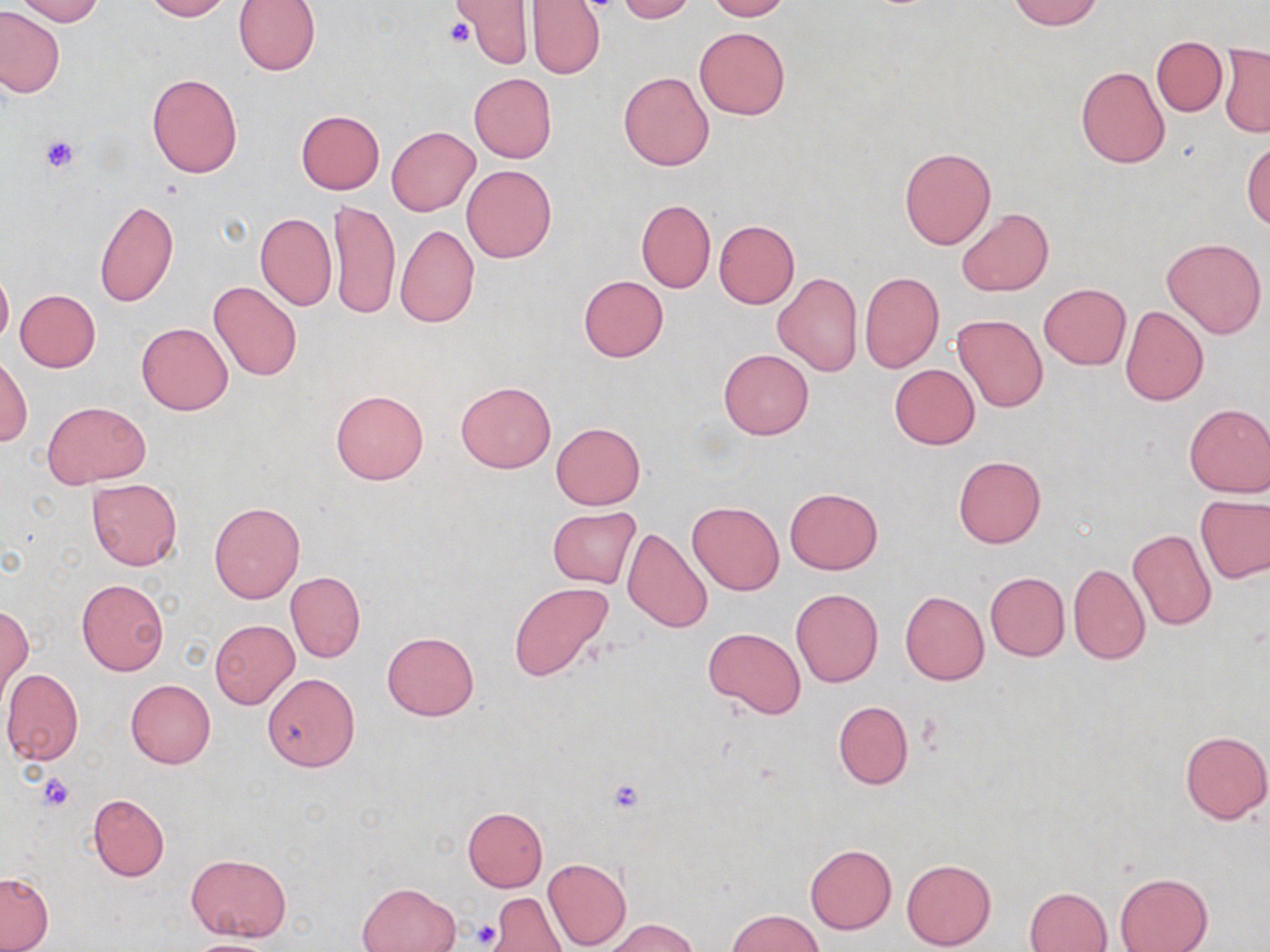

Summary:
  - Coordinate format: approximate bounding boxes as named x1/y1/x2/y2 corners in pixels
  - Platelet locations: (x1=443, y1=16, x2=475, y2=48), (x1=40, y1=134, x2=81, y2=174), (x1=39, y1=773, x2=76, y2=810), (x1=605, y1=778, x2=646, y2=814), (x1=471, y1=919, x2=503, y2=948)
  - Uninfected red blood cell locations: (x1=16, y1=0, x2=102, y2=25), (x1=141, y1=0, x2=230, y2=20), (x1=233, y1=0, x2=320, y2=74), (x1=452, y1=0, x2=532, y2=67), (x1=616, y1=0, x2=696, y2=24), (x1=706, y1=0, x2=791, y2=21), (x1=1007, y1=0, x2=1104, y2=29), (x1=526, y1=1, x2=606, y2=79), (x1=0, y1=7, x2=65, y2=99), (x1=695, y1=26, x2=789, y2=120), (x1=1152, y1=36, x2=1226, y2=116), (x1=1219, y1=44, x2=1270, y2=136), (x1=1076, y1=65, x2=1170, y2=168), (x1=618, y1=72, x2=714, y2=171), (x1=146, y1=73, x2=243, y2=178), (x1=469, y1=73, x2=557, y2=162), (x1=295, y1=110, x2=385, y2=194), (x1=386, y1=126, x2=479, y2=215), (x1=1243, y1=140, x2=1270, y2=229), (x1=899, y1=146, x2=996, y2=250), (x1=463, y1=165, x2=557, y2=263), (x1=637, y1=198, x2=715, y2=293), (x1=95, y1=199, x2=178, y2=307), (x1=328, y1=199, x2=401, y2=322), (x1=957, y1=208, x2=1053, y2=296), (x1=255, y1=212, x2=337, y2=311), (x1=714, y1=220, x2=799, y2=308), (x1=395, y1=224, x2=479, y2=328), (x1=1162, y1=237, x2=1267, y2=339), (x1=0, y1=267, x2=12, y2=347), (x1=860, y1=272, x2=944, y2=372), (x1=773, y1=273, x2=862, y2=376), (x1=579, y1=275, x2=668, y2=362), (x1=209, y1=280, x2=302, y2=382), (x1=1039, y1=283, x2=1130, y2=369), (x1=15, y1=289, x2=101, y2=372), (x1=1121, y1=306, x2=1208, y2=406), (x1=952, y1=313, x2=1048, y2=412), (x1=137, y1=322, x2=233, y2=414), (x1=719, y1=348, x2=813, y2=439), (x1=1, y1=357, x2=32, y2=447), (x1=889, y1=364, x2=979, y2=450), (x1=456, y1=380, x2=556, y2=472), (x1=330, y1=390, x2=428, y2=485), (x1=44, y1=401, x2=149, y2=488), (x1=1184, y1=403, x2=1270, y2=497), (x1=552, y1=422, x2=644, y2=509), (x1=953, y1=456, x2=1045, y2=548), (x1=86, y1=478, x2=182, y2=570), (x1=784, y1=487, x2=882, y2=574), (x1=1195, y1=494, x2=1270, y2=584), (x1=687, y1=500, x2=784, y2=595), (x1=209, y1=501, x2=305, y2=604), (x1=535, y1=504, x2=635, y2=667), (x1=547, y1=507, x2=641, y2=588), (x1=621, y1=528, x2=713, y2=633), (x1=1127, y1=528, x2=1217, y2=630), (x1=1067, y1=563, x2=1150, y2=664), (x1=286, y1=571, x2=366, y2=663), (x1=985, y1=572, x2=1069, y2=661), (x1=76, y1=579, x2=169, y2=676), (x1=510, y1=582, x2=612, y2=681), (x1=791, y1=589, x2=883, y2=687), (x1=900, y1=591, x2=989, y2=686), (x1=1, y1=605, x2=31, y2=697), (x1=210, y1=621, x2=299, y2=708), (x1=703, y1=626, x2=807, y2=718), (x1=382, y1=632, x2=479, y2=721), (x1=1, y1=669, x2=84, y2=764), (x1=262, y1=673, x2=359, y2=772), (x1=125, y1=679, x2=216, y2=769), (x1=833, y1=700, x2=913, y2=789), (x1=1180, y1=730, x2=1270, y2=824), (x1=89, y1=794, x2=169, y2=881), (x1=462, y1=807, x2=548, y2=891), (x1=805, y1=844, x2=897, y2=933), (x1=187, y1=853, x2=290, y2=942), (x1=542, y1=857, x2=632, y2=950), (x1=901, y1=858, x2=996, y2=950), (x1=0, y1=872, x2=54, y2=951), (x1=1115, y1=873, x2=1212, y2=952), (x1=356, y1=881, x2=461, y2=952), (x1=1025, y1=887, x2=1111, y2=952), (x1=490, y1=893, x2=564, y2=951), (x1=726, y1=909, x2=823, y2=951), (x1=602, y1=918, x2=695, y2=952), (x1=183, y1=938, x2=282, y2=952)
  - Slide-level diagnosis: negative for blood parasites
  - Field of view: single
  - Preparation: thin blood smear
  - Image size: 1270×952 pixels
  - Modality: optical microscopy
  - Stain: May-Grünwald-Giemsa
  - Magnification: 1000x